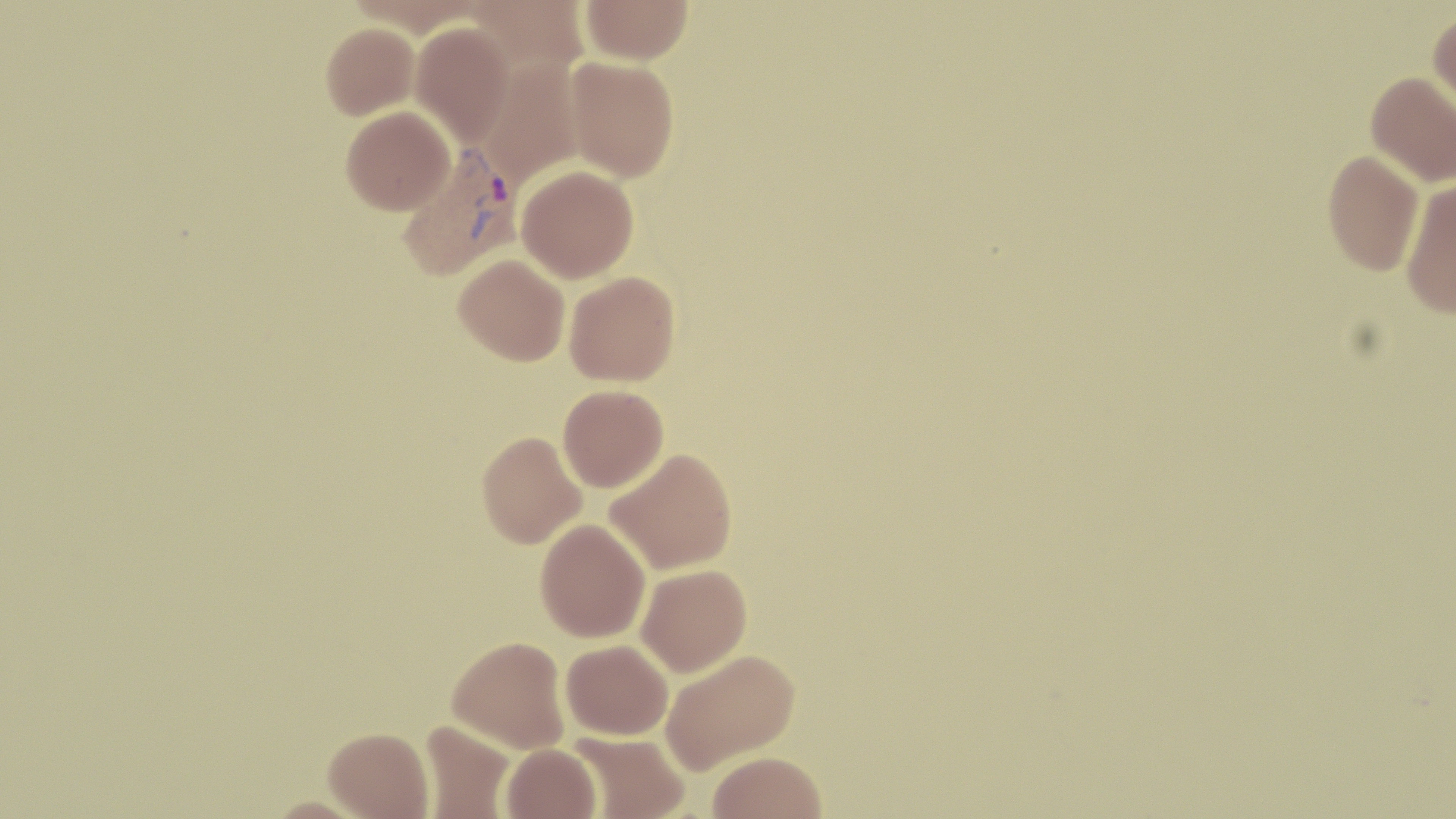
{
  "slide_level_diagnosis": "Plasmodium vivax",
  "image_size": "1456×819 pixels",
  "stain": "May-Grünwald-Giemsa",
  "plasmodium_vivax_infected_red_blood_cell_locations": "approximate bounding boxes as (x1, y1, x2, y2) in pixels: (396, 145, 521, 282)",
  "field_of_view": "single",
  "modality": "light microscopy",
  "preparation": "thin blood smear",
  "magnification": "1000x",
  "uninfected_red_blood_cell_locations": "approximate bounding boxes as (x1, y1, x2, y2) in pixels: (466, 0, 588, 76), (581, 0, 693, 64), (1428, 9, 1456, 114), (410, 22, 515, 146), (321, 23, 419, 119), (565, 56, 679, 181), (478, 59, 583, 186), (1366, 71, 1456, 187), (340, 106, 454, 214), (1322, 150, 1424, 275), (516, 165, 638, 283), (1401, 180, 1456, 319), (454, 254, 570, 366), (564, 271, 680, 386), (558, 384, 669, 492), (477, 431, 587, 548), (605, 448, 738, 574), (535, 518, 650, 642), (636, 564, 752, 677), (448, 635, 569, 753), (561, 639, 673, 739), (661, 649, 799, 773), (420, 720, 515, 818), (324, 727, 433, 819), (568, 732, 690, 818), (501, 743, 601, 819), (708, 751, 827, 819), (261, 796, 373, 819)"
}